Classify this cell by malaria status.
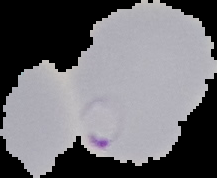

It is parasitized.

Summary:
  - Image type: segmented cell region with the area outside set to black
  - Preparation: thin blood smear
  - Image size: 217×178 pixels